Name the blood parasite species.
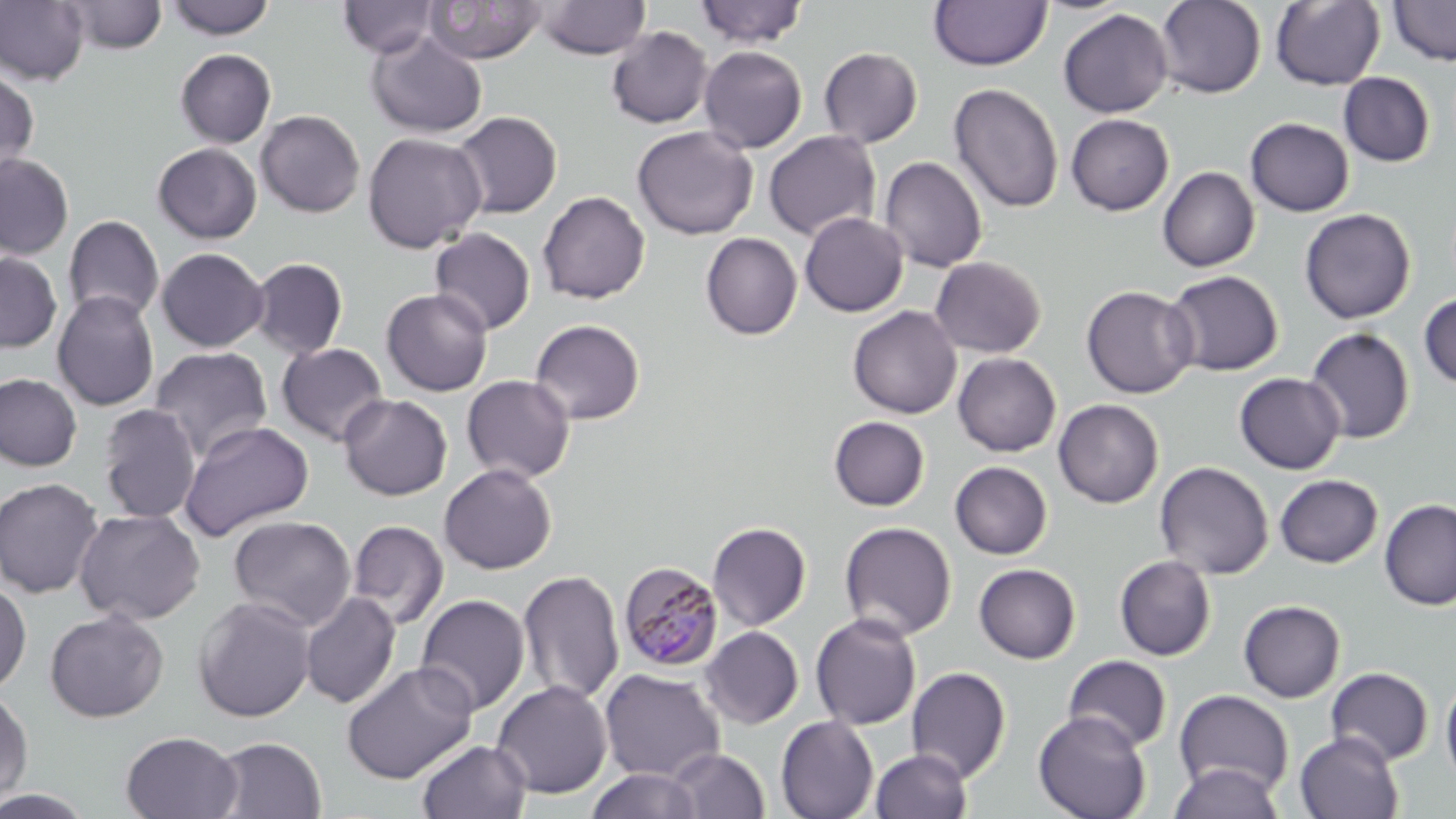
Plasmodium malariae.

Approximate bounding boxes as [x1, y1, x2, y2] in pixels. Uninfected red blood cell locations: [165, 0, 274, 40], [338, 0, 441, 59], [536, 0, 651, 59], [929, 0, 1052, 71], [1155, 0, 1266, 98], [1271, 0, 1386, 91], [0, 1, 90, 86], [61, 1, 168, 53], [423, 1, 547, 64], [694, 1, 809, 48], [1388, 1, 1456, 66], [1058, 8, 1173, 118], [606, 26, 713, 128], [365, 31, 487, 138], [699, 46, 807, 153], [819, 47, 923, 147], [175, 49, 276, 148], [0, 66, 40, 180], [1339, 72, 1435, 167], [949, 83, 1064, 213], [255, 110, 365, 217], [451, 111, 562, 218], [1066, 114, 1174, 215], [1245, 117, 1354, 216], [632, 125, 758, 239], [763, 130, 882, 241], [362, 132, 487, 253], [152, 143, 262, 243], [0, 152, 75, 260], [879, 156, 987, 272], [1157, 166, 1260, 272], [538, 190, 651, 304], [1299, 208, 1416, 324], [799, 212, 908, 317], [63, 215, 165, 324], [429, 228, 536, 335], [700, 233, 803, 340], [156, 247, 268, 352], [0, 252, 62, 353], [930, 256, 1046, 358], [249, 257, 348, 359], [1164, 270, 1283, 376], [1081, 285, 1198, 398], [380, 288, 493, 396], [52, 290, 160, 411], [1419, 293, 1456, 390], [847, 306, 962, 418], [530, 318, 646, 424], [1305, 327, 1415, 444], [276, 342, 389, 446], [149, 347, 273, 461], [953, 352, 1061, 457], [0, 373, 83, 472], [1234, 373, 1345, 474], [461, 374, 575, 484], [338, 394, 452, 500], [1053, 399, 1163, 508], [97, 404, 201, 523], [828, 416, 930, 511], [179, 420, 314, 542], [950, 461, 1053, 559], [1155, 461, 1274, 579], [439, 463, 557, 575], [1274, 474, 1383, 568], [0, 477, 104, 599], [1379, 499, 1455, 611], [73, 508, 206, 625], [229, 516, 356, 630], [347, 519, 449, 629], [839, 521, 956, 640], [707, 522, 812, 631], [1114, 555, 1217, 661], [973, 563, 1081, 664], [518, 570, 625, 705], [0, 582, 31, 694], [300, 591, 401, 709], [415, 594, 530, 716], [191, 597, 317, 722], [1239, 600, 1345, 702], [45, 609, 169, 722], [810, 612, 922, 730], [700, 626, 804, 729], [1063, 655, 1172, 752], [341, 661, 478, 784], [906, 666, 1012, 782], [1326, 667, 1434, 766], [599, 668, 726, 782], [1440, 674, 1456, 787], [491, 680, 613, 799], [0, 689, 33, 806], [1174, 689, 1294, 798], [1033, 710, 1152, 819], [776, 716, 879, 819], [121, 731, 243, 817], [1294, 731, 1404, 819], [210, 736, 327, 818], [416, 739, 532, 819], [666, 748, 771, 819], [870, 748, 972, 819], [1168, 763, 1285, 818], [586, 768, 702, 819], [0, 788, 97, 818]. Plasmodium malariae-infected red blood cell locations: [618, 560, 724, 672]. Image is 1456×819 pixels. May-Grünwald-Giemsa stain. Optical microscopy. Thin blood film. 1000x magnification. One field of a larger specimen.